Outline each blood parasite and name the species.
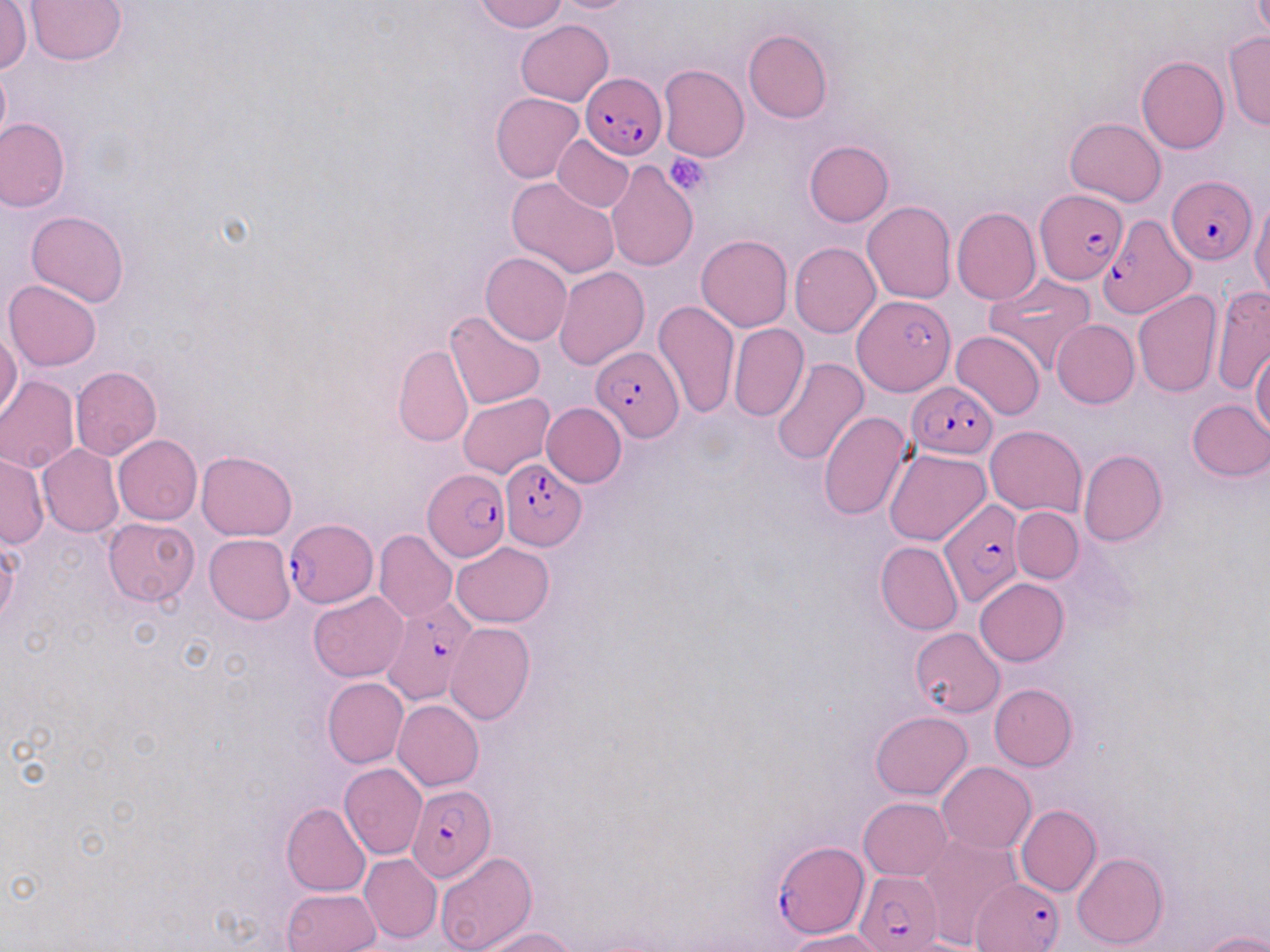

Approximate bounding boxes as [x1, y1, x2, y2] in pixels.
Plasmodium falciparum-infected red blood cells: [581, 71, 666, 160], [1169, 175, 1258, 265], [1032, 188, 1125, 283], [1099, 213, 1198, 317], [854, 294, 955, 395], [591, 345, 685, 441], [907, 380, 998, 458], [500, 456, 586, 548], [421, 468, 509, 562], [939, 498, 1023, 609], [284, 519, 377, 609], [381, 598, 476, 704], [405, 785, 494, 882], [776, 842, 867, 938], [855, 869, 943, 950], [973, 879, 1063, 951].
No Plasmodium ovale, Plasmodium malariae, Plasmodium vivax, Babesia divergens, or Trypanosoma brucei observed.

slide_level_diagnosis: Plasmodium falciparum
platelet_locations: 'approximate bounding boxes as [x1, y1, x2, y2] in pixels: [664, 153, 710, 197]'
uninfected_red_blood_cell_locations: 'approximate bounding boxes as [x1, y1, x2, y2] in pixels: [25, 0, 128, 65], [475, 0, 567, 33], [548, 0, 644, 13], [1, 3, 32, 74], [516, 19, 613, 105], [743, 30, 831, 124], [1222, 31, 1270, 130], [1136, 55, 1229, 153], [0, 62, 10, 155], [658, 64, 749, 162], [491, 92, 584, 184], [0, 116, 70, 212], [1065, 116, 1167, 206], [552, 135, 634, 212], [803, 140, 893, 227], [607, 162, 698, 271], [506, 177, 621, 278], [1250, 198, 1270, 301], [862, 200, 956, 303], [952, 207, 1041, 306], [26, 210, 128, 307], [696, 235, 793, 332], [789, 242, 881, 338], [481, 251, 572, 345], [553, 267, 650, 367], [983, 274, 1096, 375], [3, 279, 101, 371], [1210, 285, 1270, 395], [1133, 289, 1224, 398], [654, 300, 740, 419], [444, 310, 548, 411], [1051, 319, 1139, 408], [727, 323, 808, 421], [0, 331, 22, 421], [950, 331, 1045, 420], [394, 344, 473, 446], [1251, 347, 1270, 440], [770, 356, 868, 466], [71, 366, 161, 460], [0, 375, 79, 472], [458, 393, 554, 478], [1187, 399, 1270, 481], [540, 402, 626, 486], [818, 412, 912, 521], [985, 425, 1087, 516], [113, 434, 202, 525], [38, 445, 123, 537], [885, 448, 992, 545], [1078, 450, 1167, 546], [197, 451, 297, 540], [0, 453, 48, 548], [1011, 506, 1084, 583], [103, 517, 199, 607], [374, 529, 456, 622], [204, 534, 294, 624], [451, 541, 554, 626], [876, 542, 963, 634], [976, 578, 1067, 665], [308, 592, 409, 683], [445, 623, 534, 723], [909, 627, 1004, 717], [322, 678, 409, 768], [989, 683, 1079, 770], [393, 700, 484, 789], [870, 712, 972, 799], [938, 761, 1036, 854], [339, 764, 427, 859], [858, 797, 952, 881], [281, 802, 372, 896], [1016, 805, 1101, 896], [917, 831, 1021, 947], [436, 851, 538, 950], [359, 853, 442, 943], [1072, 853, 1169, 948], [283, 888, 381, 952], [475, 927, 579, 952], [785, 930, 889, 952], [1198, 930, 1270, 952]'
magnification: 1000x
preparation: thin blood smear
field_of_view: single
modality: optical microscopy
stain: May-Grünwald-Giemsa
image_size: 1270×952 pixels